Locate every blood parasite and identify its species.
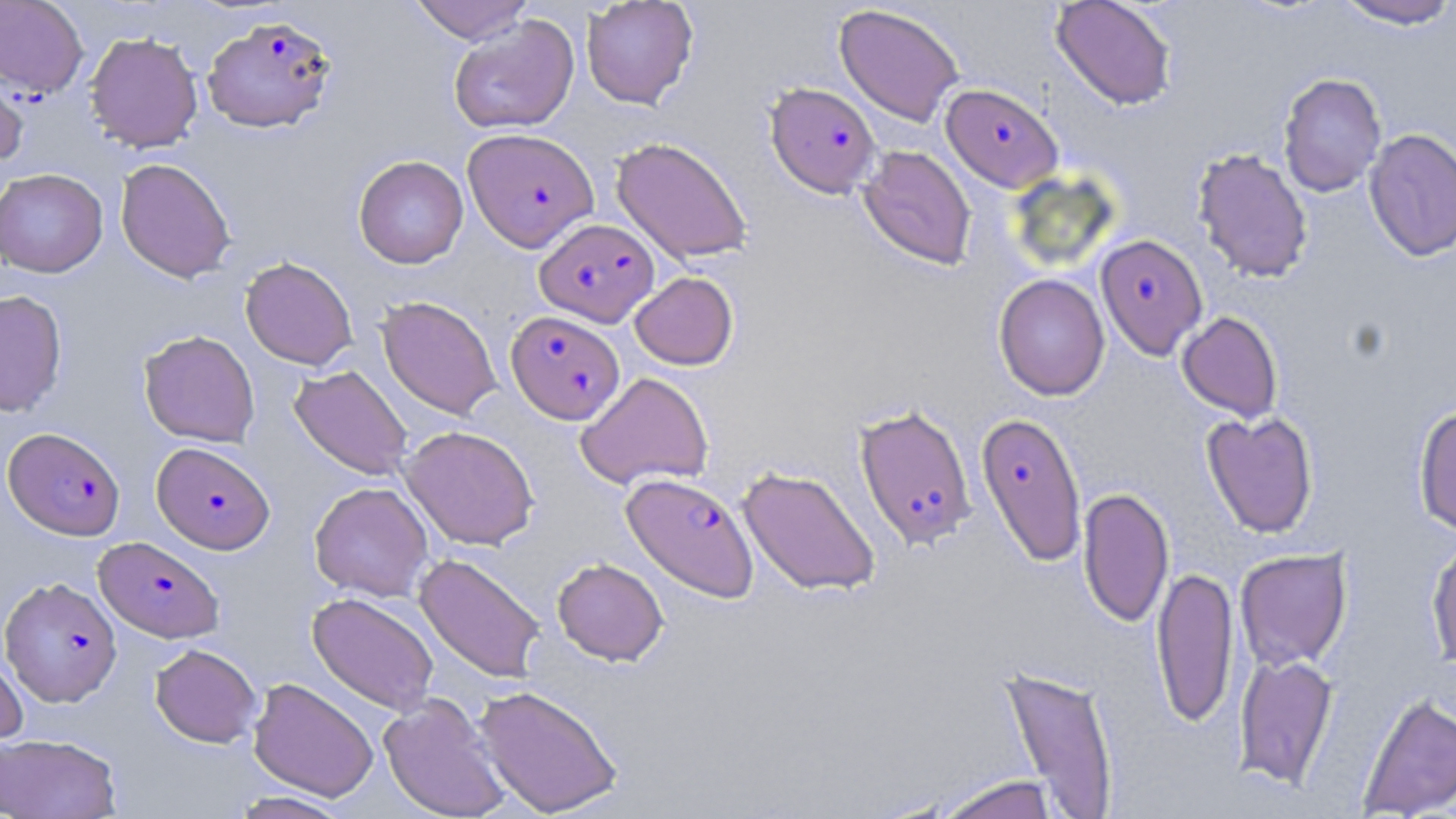
Approximate bounding boxes as (x1, y1, x2, y2) in pixels.
Plasmodium falciparum-infected red blood cells: (202, 15, 336, 133), (765, 82, 880, 197), (941, 83, 1063, 192), (463, 127, 598, 251), (535, 218, 659, 327), (1095, 233, 1208, 359), (506, 310, 625, 424), (854, 404, 977, 550), (975, 411, 1087, 566), (3, 427, 125, 540), (152, 441, 275, 554), (621, 472, 759, 602), (94, 536, 224, 643), (1, 576, 122, 707).
No Plasmodium ovale, Plasmodium malariae, Plasmodium vivax, Babesia divergens, or Trypanosoma brucei observed.

slide-level diagnosis = Plasmodium falciparum
image size = 1456×819 pixels
uninfected red blood cell locations = approximate bounding boxes as (x1, y1, x2, y2) in pixels: (0, 0, 88, 98), (409, 0, 535, 44), (582, 0, 698, 109), (1050, 0, 1177, 110), (1332, 0, 1456, 30), (834, 4, 964, 126), (448, 15, 580, 135), (84, 31, 203, 153), (0, 64, 29, 171), (1278, 72, 1387, 197), (1364, 128, 1456, 262), (611, 136, 753, 265), (858, 145, 977, 270), (1192, 148, 1313, 283), (353, 155, 468, 269), (115, 158, 235, 283), (0, 168, 108, 277), (240, 256, 358, 371), (630, 272, 738, 370), (994, 273, 1110, 401), (0, 290, 68, 417), (377, 295, 502, 420), (1177, 311, 1283, 422), (138, 329, 260, 447), (289, 365, 413, 480), (576, 372, 713, 490), (1413, 404, 1456, 536), (1202, 411, 1319, 538), (399, 425, 540, 550), (737, 465, 881, 597), (309, 481, 434, 601), (1078, 487, 1174, 629), (1426, 534, 1456, 670), (1234, 547, 1352, 671), (414, 553, 546, 684), (552, 557, 668, 666), (1151, 565, 1239, 728), (307, 591, 439, 716), (150, 644, 262, 747), (0, 649, 28, 751), (1234, 653, 1338, 789), (996, 663, 1120, 818), (248, 677, 379, 801), (473, 684, 624, 817), (1357, 692, 1456, 818), (378, 693, 510, 819), (0, 733, 122, 818), (931, 774, 1062, 819), (230, 791, 353, 818)
modality = light microscopy
stain = May-Grünwald-Giemsa
field of view = single
preparation = thin blood film
magnification = 1000x